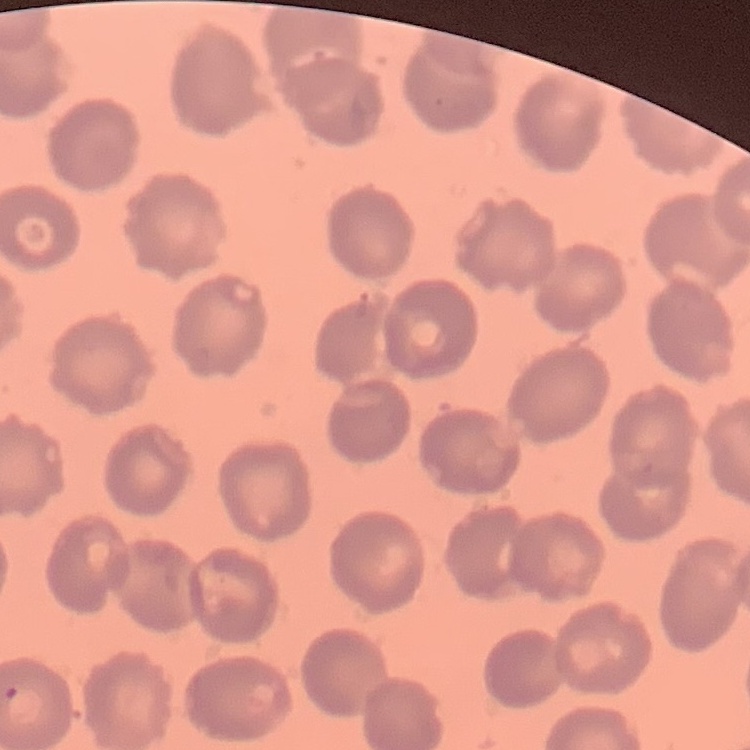

red blood cell morphology = no rouleaux formation
preparation = thin peripheral smear
stain = Field's or Giemsa
image type = one tile cut from a larger photomicrograph